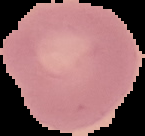

result = no Plasmodium parasites seen
preparation = thin blood smear
image type = segmented cell region with the area outside set to black
image size = 145×136 pixels